State which parasite is depicted.
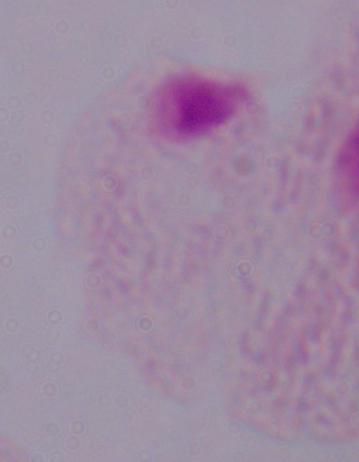
This is a trichomonad.

{
  "magnification": "1000x",
  "modality": "photomicrograph"
}